Give the preparation type.
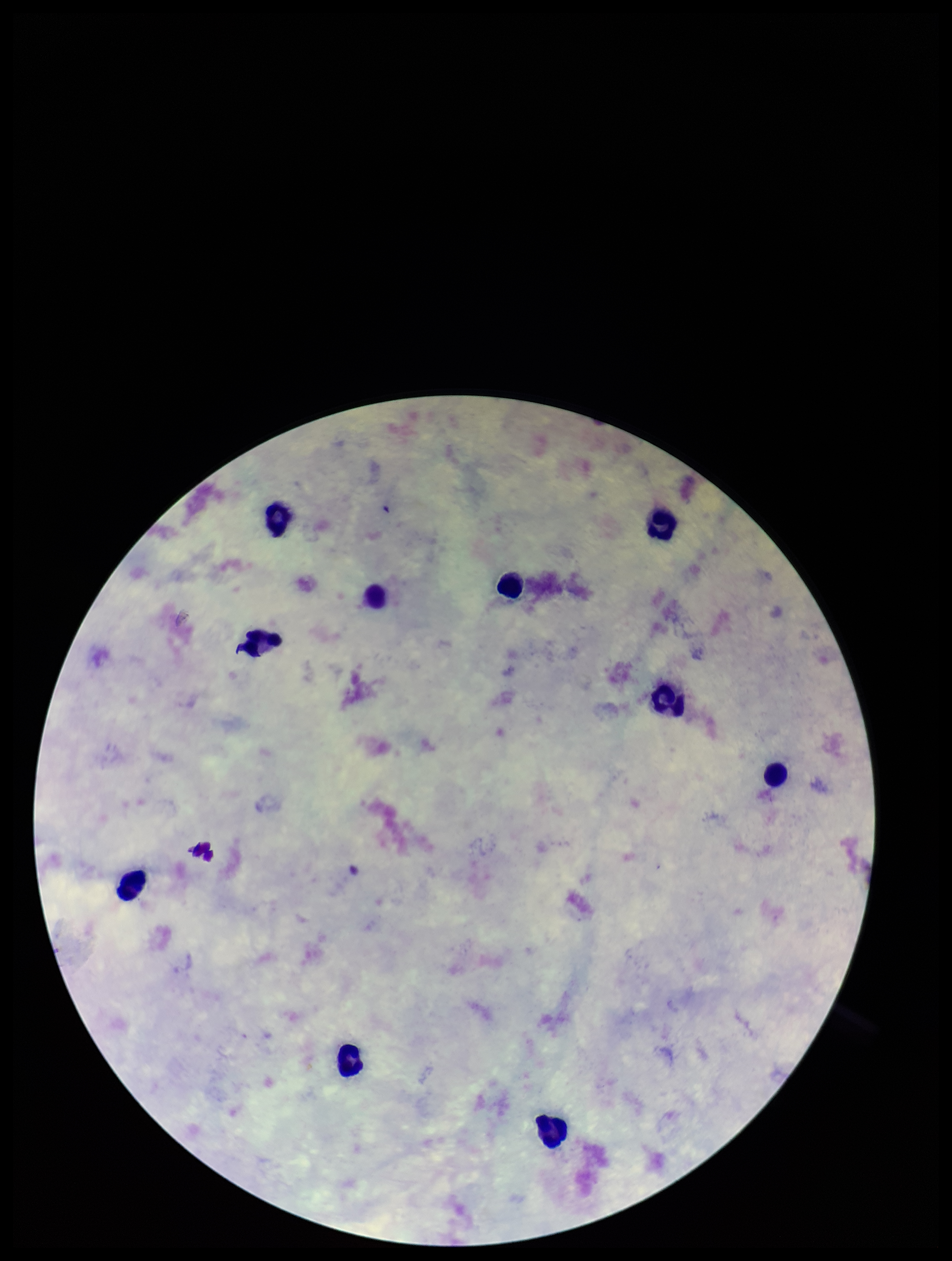
Thick.

One field from this slide. Photographed through the microscope eyepiece with a smartphone camera. Parasite count: 0. Image is 952×1261 pixels. Giemsa stain. Plasmodium parasites: none detected. Leukocyte count: 10. Patient malaria status: negative.